Outline every Plasmodium parasite, every leukocyte, and every artifact (stain precipitate or debris).
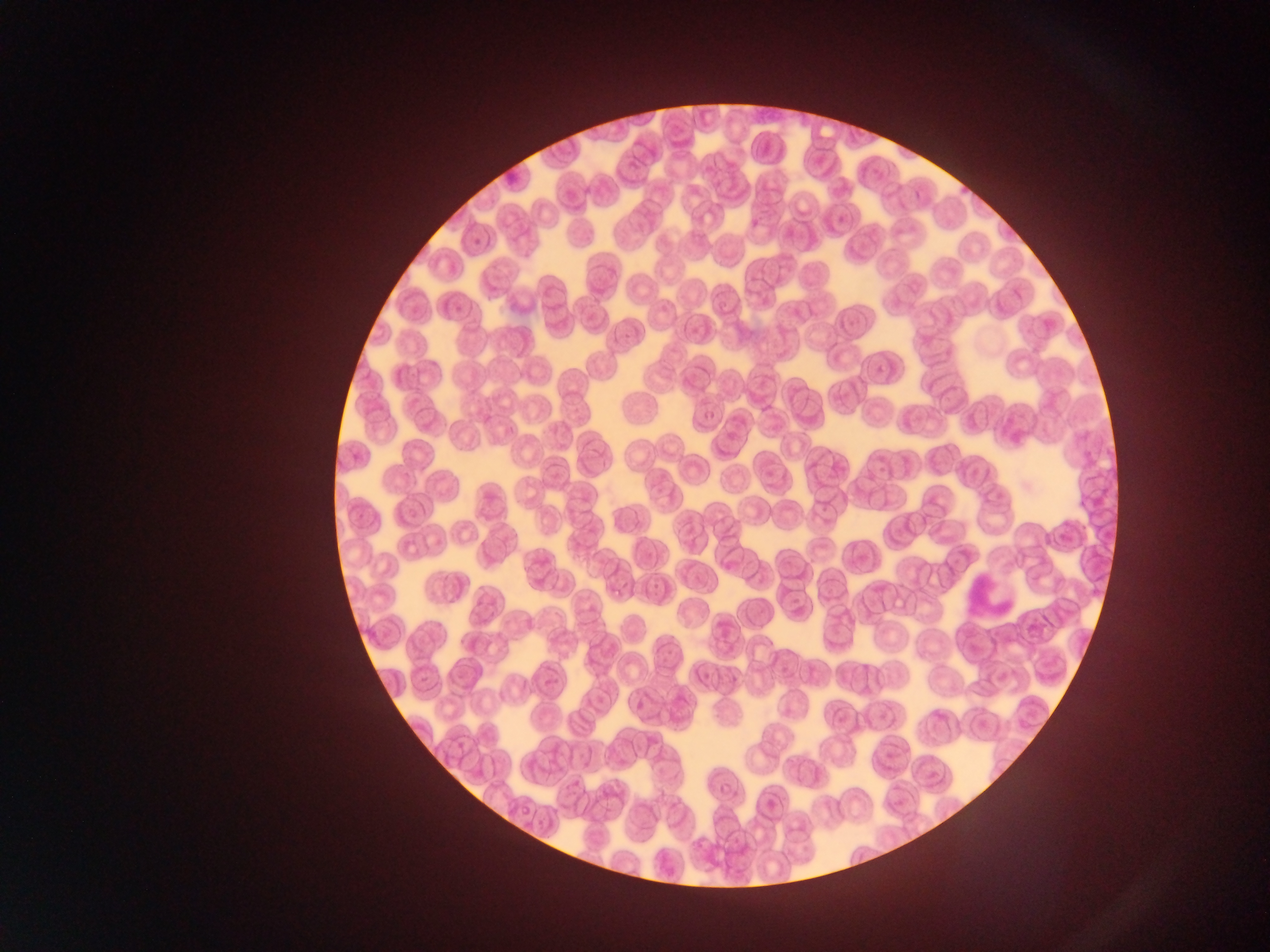
Approximate bounding boxes as {left, top, right, bottom} in pixels.
No Plasmodium parasites observed.
Leukocytes: {961, 566, 1024, 619}.

Summary:
  - Preparation: thin blood film
  - Country: Ghana
  - Capture: mobile-phone photograph through a microscope
  - Image size: 1270×952 pixels
  - Field of view: single